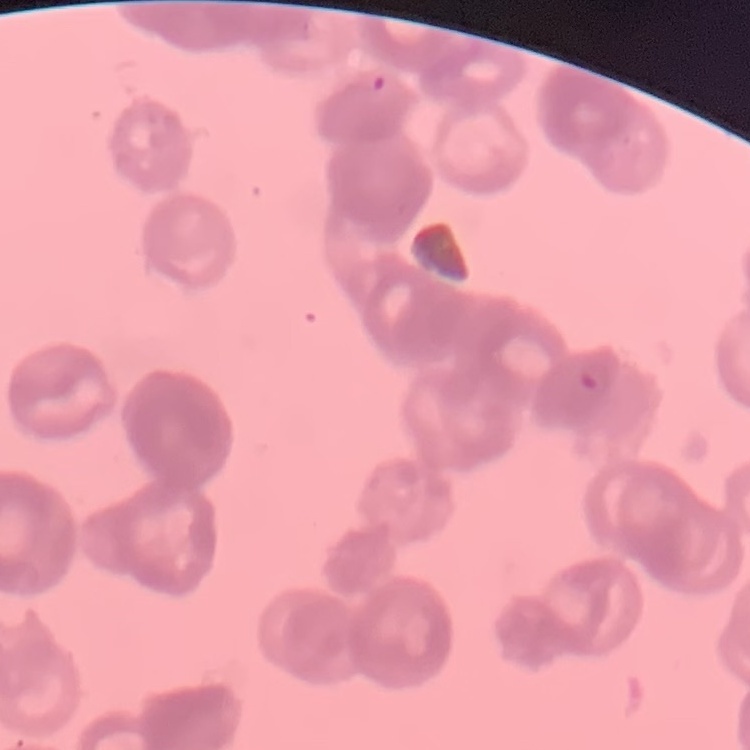

Summary:
  - Erythrocyte morphology: rouleaux formation
  - Preparation: thin blood film
  - Stain: Field's or Giemsa
  - Image type: one tile cut from a larger photomicrograph